Report the malaria status of this cell.
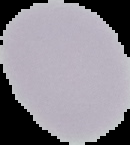

It is uninfected.

image size = 130×145 pixels
preparation = thin blood film
image type = segmented cell region with the area outside set to black